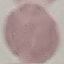

malaria_status: uninfected
preparation: thin smear
capture: smartphone camera at the microscope eyepiece
image_type: cell patch, automatically extracted from a larger field of view and resized to 64 × 64 pixels
stain: Giemsa